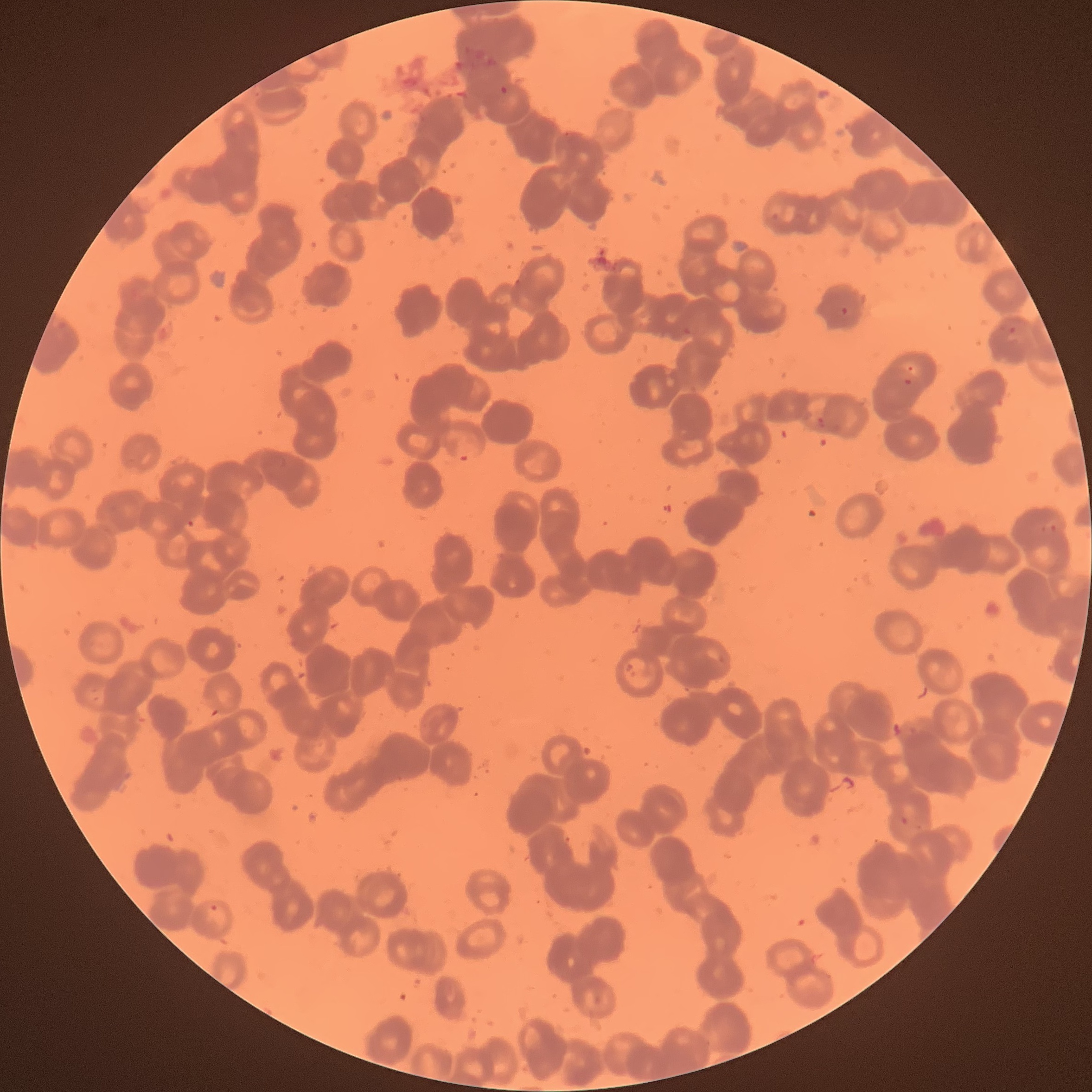
Summary:
  - Coordinate format: approximate bounding boxes as (x1, y1, x2, y2) in pixels
  - Plasmodium parasite locations: (499, 84, 513, 96), (840, 307, 849, 316), (1002, 322, 1021, 337), (903, 378, 913, 387), (814, 415, 842, 432), (454, 438, 479, 462), (1040, 520, 1058, 533), (900, 816, 924, 833), (206, 901, 231, 932)
  - Image size: 1092×1092 pixels
  - Red blood cell morphology: rouleaux formation
  - Preparation: thin blood smear
  - Modality: optical microscopy